Point out each malaria parasite and each leukocyte.
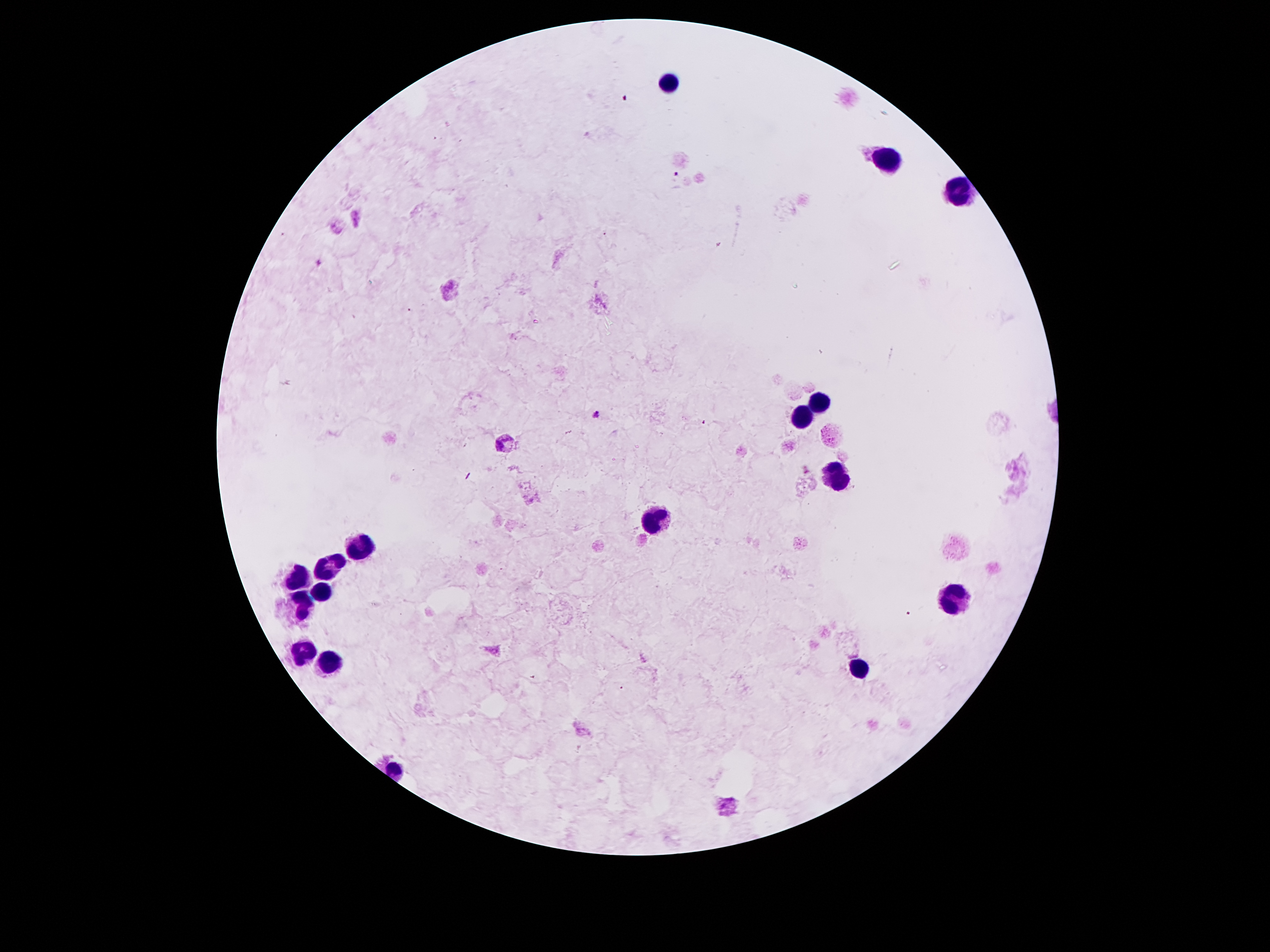
Approximate object centers, in pixels from the top-left corner.
Malaria parasites: (x=625, y=96), (x=678, y=175), (x=320, y=262), (x=597, y=414), (x=500, y=443), (x=908, y=613).
Leukocytes: (x=668, y=80), (x=887, y=163), (x=956, y=192), (x=815, y=404), (x=799, y=419), (x=839, y=476), (x=654, y=519), (x=356, y=546), (x=330, y=568), (x=299, y=575), (x=322, y=587), (x=954, y=598), (x=301, y=604), (x=305, y=653), (x=328, y=663), (x=862, y=669).

Summary:
  - Patient malaria status: positive for Plasmodium falciparum
  - Stain: Giemsa
  - Magnification: 100x
  - Preparation: thick blood film
  - Field of view: single
  - Capture: smartphone through the microscope eyepiece
  - Image size: 1270×952 pixels